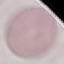
Result: no malaria parasites detected. Giemsa stain. Photographed with a smartphone camera at the microscope eyepiece. Thin blood film. Automatically extracted cell patch, resized to 64 × 64 pixels.